State which cell type is depicted.
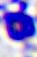
This is a leukocyte.

Micrograph. Captured at 400x magnification.